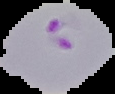
Summary:
  - Preparation: thin blood film
  - Image size: 115×94 pixels
  - Image type: segmented cell region on a black background
  - Result: malaria parasites detected